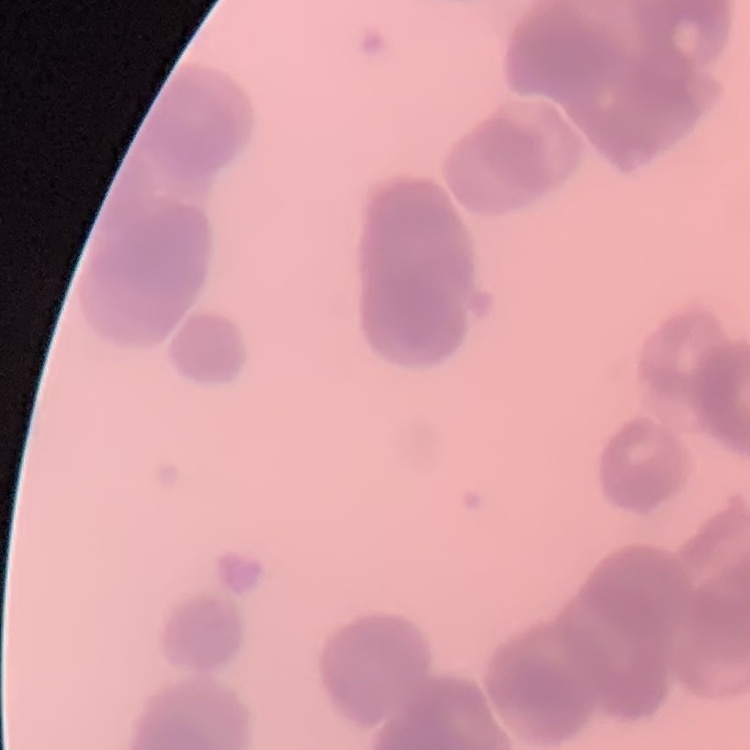

The erythrocytes exhibit rouleaux formation. Square crop of a larger photomicrograph. Thin peripheral smear. Field's or Giemsa stain.